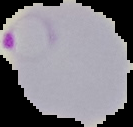
Summary:
  - Preparation: thin blood film
  - Image type: cell region segmented out of the field of view; surrounding area masked to black
  - Image size: 133×127 pixels
  - Malaria status: parasitized